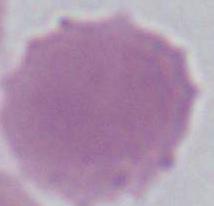

Summary:
  - Identification: red blood cell
  - Modality: photomicrograph
  - Magnification: 1000x